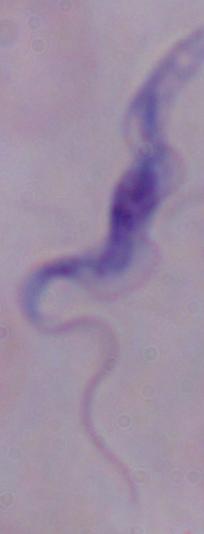
Micrograph. Captured at 1000x magnification. A trypanosome is seen.